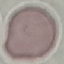
malaria status = uninfected
preparation = thin blood smear
image type = cell patch, automatically extracted from a larger field of view and resized to 64 × 64 pixels
capture = smartphone camera at the microscope eyepiece
stain = Giemsa